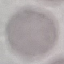

Summary:
  - Result: no malaria parasites seen
  - Capture: smartphone camera at the microscope eyepiece
  - Stain: Giemsa
  - Image type: cell patch, automatically extracted from a larger field of view and resized to 64 × 64 pixels
  - Preparation: thin blood smear